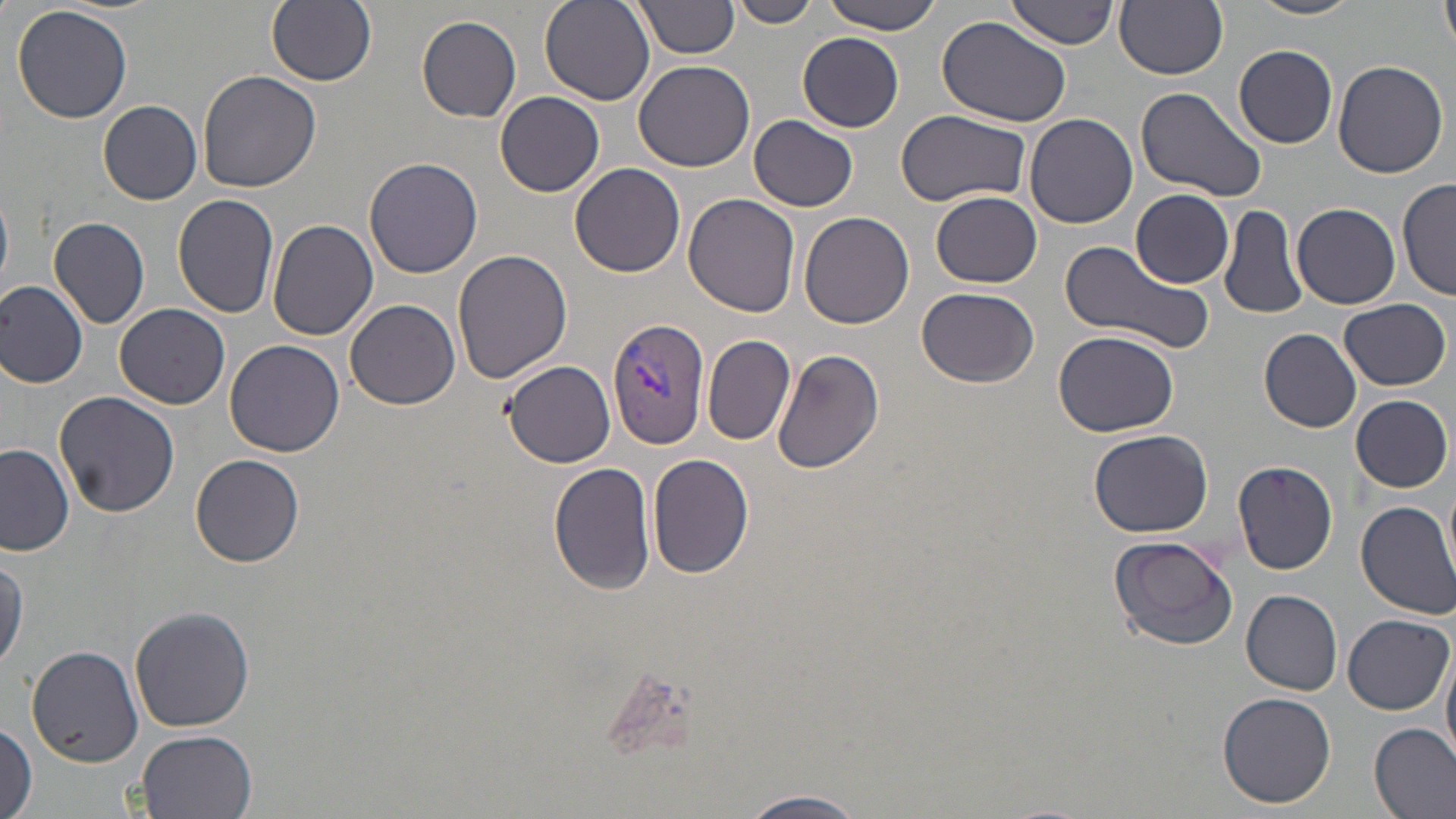 Approximate bounding boxes as (x1,y1)-(x2,y2) corner pairs in pixels. Plasmodium vivax-infected red blood cell locations: (608,316)-(711,448). Uninfected red blood cell locations: (266,0)-(377,86), (538,0)-(655,107), (636,0)-(740,58), (733,0)-(818,27), (823,0)-(945,34), (1007,0)-(1122,49), (1116,0)-(1228,79), (1248,0)-(1365,21), (1440,0)-(1456,56), (13,6)-(134,124), (416,15)-(522,123), (937,16)-(1072,127), (797,32)-(904,130), (1234,43)-(1339,149), (632,60)-(754,172), (1333,61)-(1448,179), (197,70)-(322,192), (1135,86)-(1267,204), (496,91)-(604,198), (98,99)-(203,203), (1024,110)-(1139,229), (895,111)-(1031,207), (748,116)-(859,211), (364,156)-(484,279), (569,162)-(685,277), (1398,177)-(1455,302), (1130,188)-(1235,287), (0,190)-(13,290), (931,191)-(1042,288), (172,193)-(280,319), (682,193)-(800,319), (1293,203)-(1399,310), (1218,204)-(1307,321), (799,211)-(916,328), (49,216)-(151,329), (267,219)-(378,340), (1056,239)-(1214,356), (453,247)-(573,384), (0,281)-(89,388), (916,286)-(1039,387), (1338,297)-(1451,390), (345,298)-(460,409), (115,303)-(230,409), (1054,329)-(1180,437), (1259,329)-(1362,432), (704,334)-(795,447), (225,339)-(344,457), (772,350)-(884,476), (503,360)-(616,466), (54,392)-(180,518), (1350,395)-(1453,493), (1089,429)-(1214,537), (1,443)-(74,555), (646,452)-(755,578), (192,454)-(304,567), (1231,459)-(1340,574), (551,462)-(656,594), (1442,473)-(1456,587), (1356,500)-(1456,618), (1107,534)-(1239,650), (0,552)-(28,673), (1241,588)-(1343,694), (129,605)-(254,732), (1343,614)-(1452,714), (1442,643)-(1456,767), (26,644)-(145,766), (1218,692)-(1336,810), (1370,722)-(1456,819), (0,723)-(37,818), (135,729)-(257,819), (739,791)-(872,818). Slide-level diagnosis: Plasmodium vivax. Light microscopy. 1000x magnification. One field of a larger specimen. May-Grünwald-Giemsa-stained preparation. Thin blood smear. Image is 1456×819 pixels.